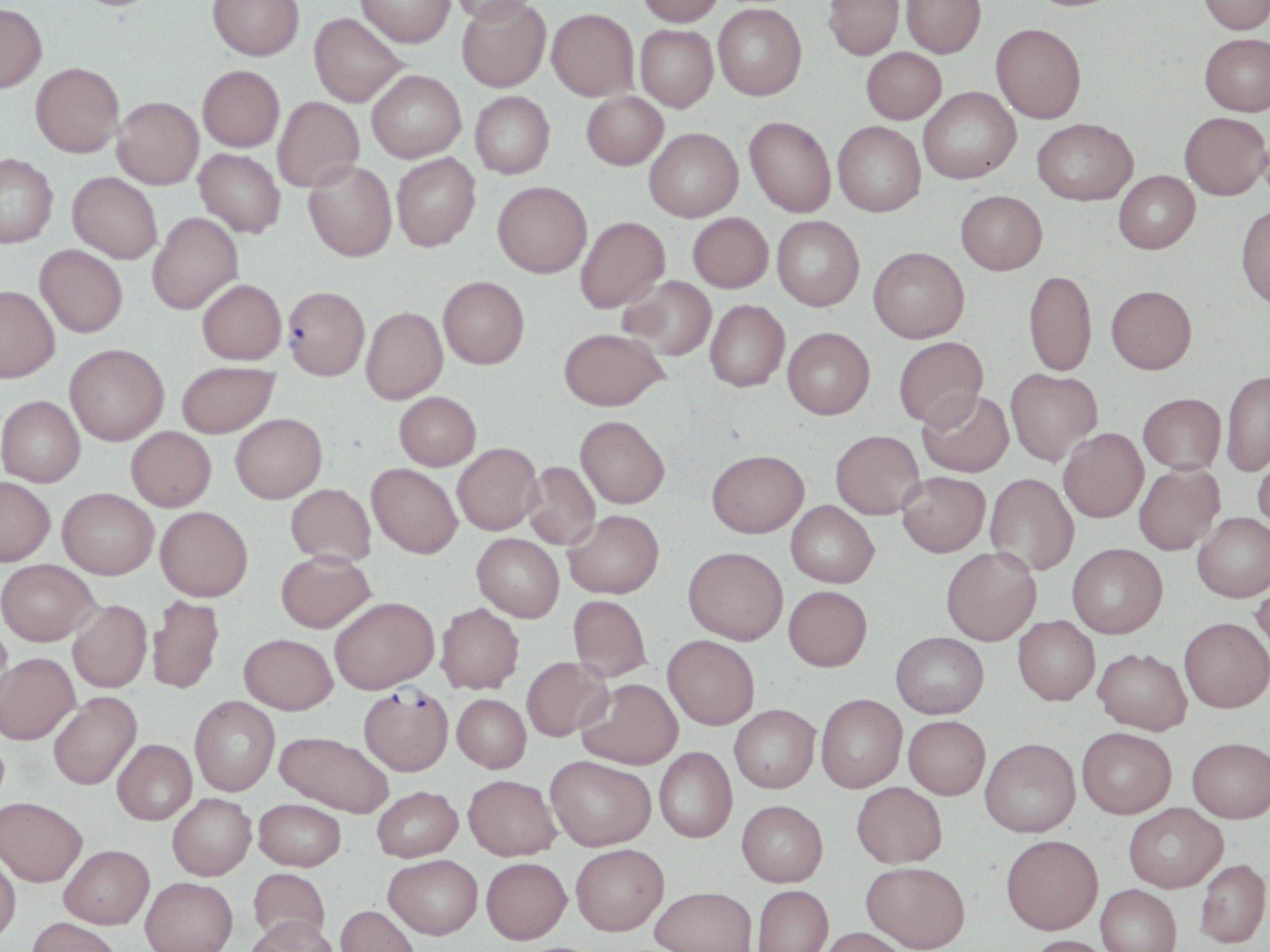
{
  "slide_level_diagnosis": "Plasmodium falciparum",
  "uninfected_red_blood_cell_locations": "approximate bounding boxes as [x1, y1, x2, y2] in pixels: [208, 0, 304, 60], [357, 0, 455, 47], [449, 0, 537, 26], [456, 0, 551, 92], [637, 0, 724, 26], [823, 0, 904, 60], [901, 0, 986, 57], [1199, 0, 1270, 35], [0, 3, 47, 93], [713, 3, 807, 100], [547, 8, 638, 100], [309, 12, 408, 107], [990, 23, 1086, 123], [635, 25, 718, 112], [1200, 33, 1270, 116], [861, 47, 946, 123], [31, 62, 124, 157], [198, 65, 285, 152], [367, 69, 466, 163], [919, 86, 1020, 184], [470, 91, 555, 178], [582, 92, 668, 170], [273, 96, 364, 191], [113, 97, 204, 189], [1179, 112, 1270, 200], [745, 116, 836, 217], [1032, 118, 1137, 205], [833, 120, 926, 216], [645, 128, 743, 221], [194, 148, 285, 238], [391, 152, 481, 251], [0, 153, 58, 248], [303, 161, 397, 261], [1113, 170, 1200, 254], [67, 172, 162, 263], [493, 181, 592, 278], [956, 190, 1047, 274], [1236, 204, 1270, 309], [147, 212, 243, 314], [688, 212, 773, 292], [772, 215, 864, 311], [575, 216, 670, 313], [35, 245, 127, 337], [869, 246, 969, 342], [1024, 270, 1096, 376], [438, 276, 529, 369], [620, 276, 717, 361], [197, 279, 286, 364], [0, 285, 60, 382], [1106, 285, 1197, 374], [705, 299, 789, 391], [361, 306, 447, 404], [559, 327, 668, 410], [783, 327, 875, 419], [894, 336, 988, 429], [65, 343, 169, 445], [177, 361, 278, 438], [1005, 368, 1101, 465], [1222, 369, 1270, 476], [918, 390, 1014, 477], [394, 391, 480, 470], [1138, 393, 1226, 474], [0, 395, 85, 487], [230, 413, 327, 503], [576, 415, 670, 508], [126, 426, 216, 511], [1058, 428, 1148, 522], [830, 430, 925, 519], [452, 443, 543, 534], [1252, 443, 1270, 533], [707, 449, 809, 537], [524, 461, 601, 549], [367, 463, 462, 558], [1134, 464, 1224, 554], [897, 472, 990, 556], [985, 473, 1079, 576], [0, 476, 55, 566], [286, 483, 376, 566], [58, 487, 159, 579], [786, 501, 878, 587], [156, 506, 253, 601], [564, 509, 664, 598], [1193, 512, 1270, 602], [473, 533, 564, 621], [1067, 543, 1167, 638], [684, 546, 788, 644], [941, 547, 1041, 645], [276, 551, 375, 632], [0, 559, 100, 645], [1251, 576, 1270, 667], [784, 585, 872, 670], [568, 595, 651, 680], [147, 596, 224, 693], [329, 596, 438, 694], [68, 600, 152, 692], [436, 603, 524, 694], [1013, 615, 1099, 705], [1179, 617, 1270, 712], [0, 623, 12, 714], [891, 631, 989, 718], [239, 633, 337, 714], [663, 635, 759, 729], [1094, 647, 1192, 734], [0, 652, 80, 744], [521, 656, 612, 741], [578, 678, 683, 769], [49, 692, 142, 789], [816, 693, 907, 792], [452, 694, 531, 772], [190, 696, 280, 795], [730, 704, 820, 792], [904, 715, 990, 799], [1077, 727, 1176, 818], [275, 730, 394, 817], [980, 737, 1080, 836], [1187, 737, 1270, 822], [112, 739, 197, 824], [654, 747, 736, 842], [545, 755, 655, 850], [464, 774, 560, 860], [852, 782, 947, 868], [372, 785, 463, 861], [168, 793, 256, 879], [0, 797, 87, 886], [254, 798, 346, 870], [737, 800, 828, 886], [1124, 802, 1227, 892], [1002, 834, 1103, 934], [571, 843, 669, 935], [59, 844, 154, 929], [0, 852, 21, 942], [384, 854, 482, 938], [481, 856, 571, 943], [1195, 858, 1270, 948], [861, 861, 970, 951], [248, 867, 330, 945], [141, 876, 237, 952], [1096, 884, 1181, 952], [752, 885, 833, 952], [650, 886, 756, 952], [335, 904, 420, 952], [246, 916, 340, 952], [27, 917, 123, 952], [818, 927, 912, 952], [1025, 935, 1114, 952]",
  "modality": "optical microscopy",
  "stain": "May-Grünwald-Giemsa",
  "image_size": "1270×952 pixels",
  "plasmodium_falciparum_infected_red_blood_cell_locations": "approximate bounding boxes as [x1, y1, x2, y2] in pixels: [283, 286, 369, 380], [358, 686, 454, 776]",
  "field_of_view": "single",
  "magnification": "1000x",
  "preparation": "thin blood film"
}